Name the parasite shown.
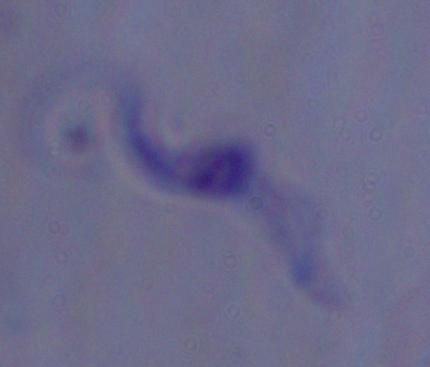
A trypanosome.

{
  "magnification": "1000x",
  "modality": "micrograph"
}